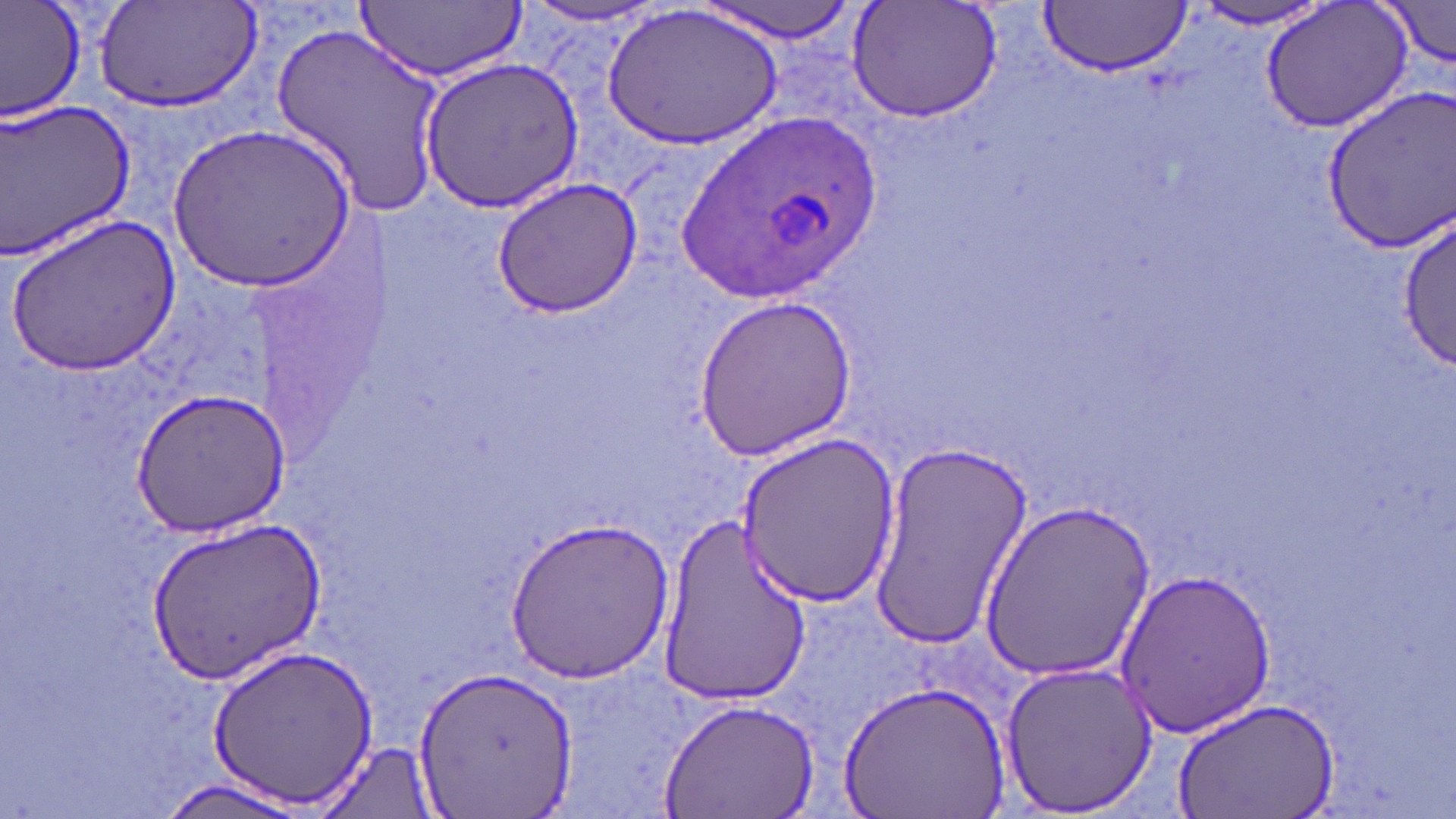

Summary:
  - Coordinate format: approximate bounding boxes as (x1,y1)-(x2,y2) corner pairs in pixels
  - Uninfected red blood cell locations: (0,0)-(87,122), (93,0)-(264,118), (354,0)-(525,82), (1258,0)-(1412,133), (1379,0)-(1456,69), (696,1)-(861,42), (1038,1)-(1193,76), (846,2)-(1003,123), (518,3)-(669,28), (605,3)-(783,148), (1186,3)-(1337,32), (270,23)-(449,213), (420,58)-(586,209), (1321,88)-(1456,251), (0,100)-(139,258), (165,123)-(353,290), (490,177)-(643,316), (1399,212)-(1452,371), (10,214)-(180,376), (693,293)-(857,458), (130,389)-(289,536), (736,429)-(902,606), (867,441)-(1034,649), (979,499)-(1154,680), (658,513)-(813,701), (503,515)-(676,683), (147,516)-(324,680), (1115,566)-(1277,739), (210,642)-(377,811), (998,659)-(1161,814), (416,666)-(577,813), (840,679)-(1009,818), (662,698)-(818,818), (1174,698)-(1340,819), (318,742)-(441,819), (155,777)-(316,818)
  - Plasmodium ovale-infected red blood cell locations: (685,109)-(880,304)
  - Slide-level diagnosis: Plasmodium ovale
  - Stain: May-Grünwald-Giemsa
  - Magnification: 1000x
  - Image size: 1456×819 pixels
  - Field of view: single
  - Modality: optical microscopy
  - Preparation: thin blood film